Locate every Plasmodium parasite by life-cycle stage, and every leukocyte.
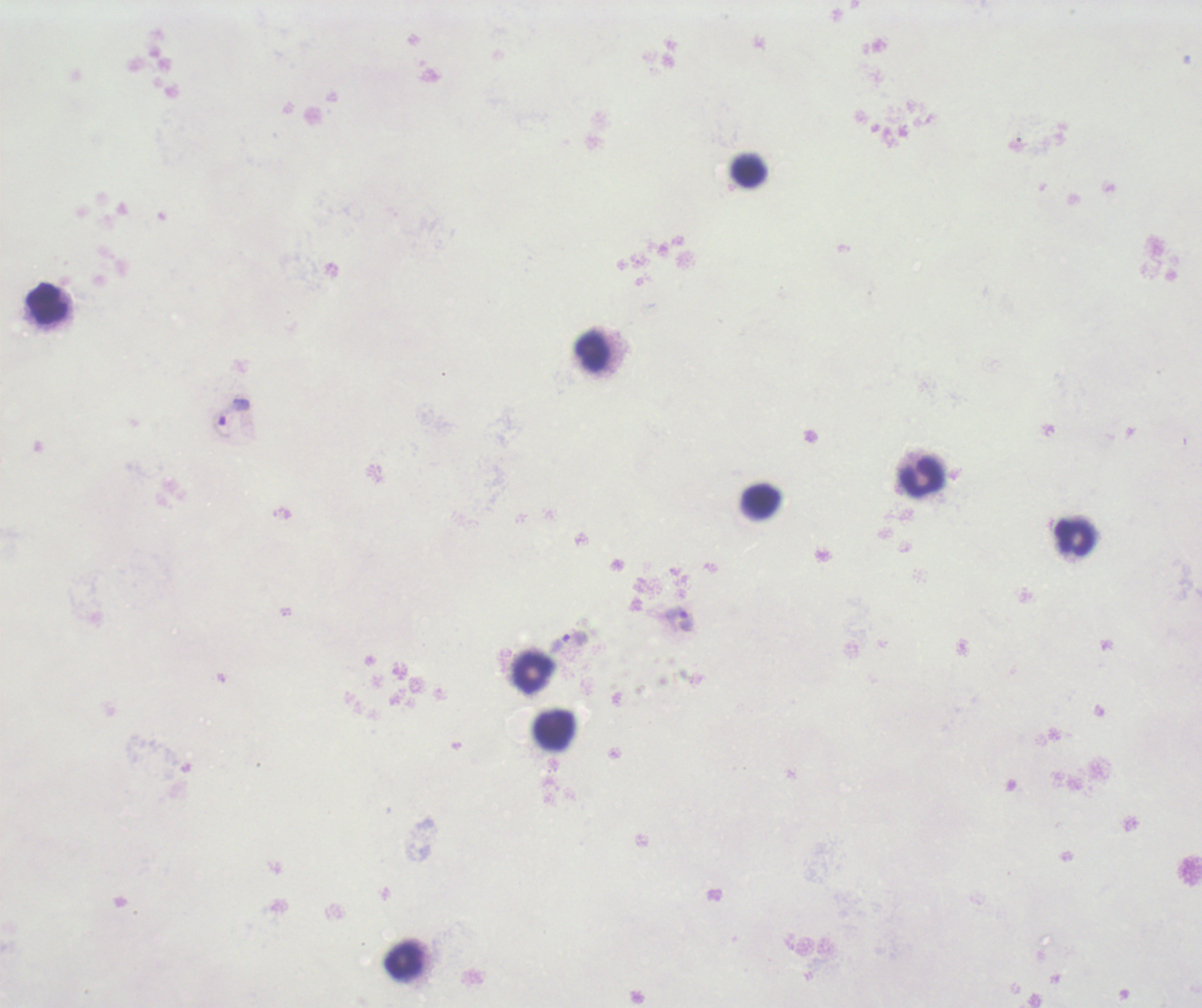
Approximate centers as [x, y] in pixels.
Trophozoites: [234, 412], [677, 619], [570, 641].
No schizont or gametocyte forms observed.
Leukocytes: [748, 172], [47, 303], [594, 354], [919, 477], [760, 502], [1073, 537], [532, 672], [554, 730], [405, 962].

magnification: 100x
context: previously used in an actual diagnosis
field_of_view: single
background_quality: unsatisfactory
stain: Romanowsky
coloration_quality: bad
preparation: thick smear of blood
image_size: 1202×1008 pixels